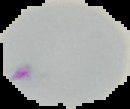
Summary:
  - Preparation: thin blood film
  - Image size: 130×109 pixels
  - Image type: segmented cell region on a black background
  - Malaria status: parasitized